Describe the morphology of the red blood cells.
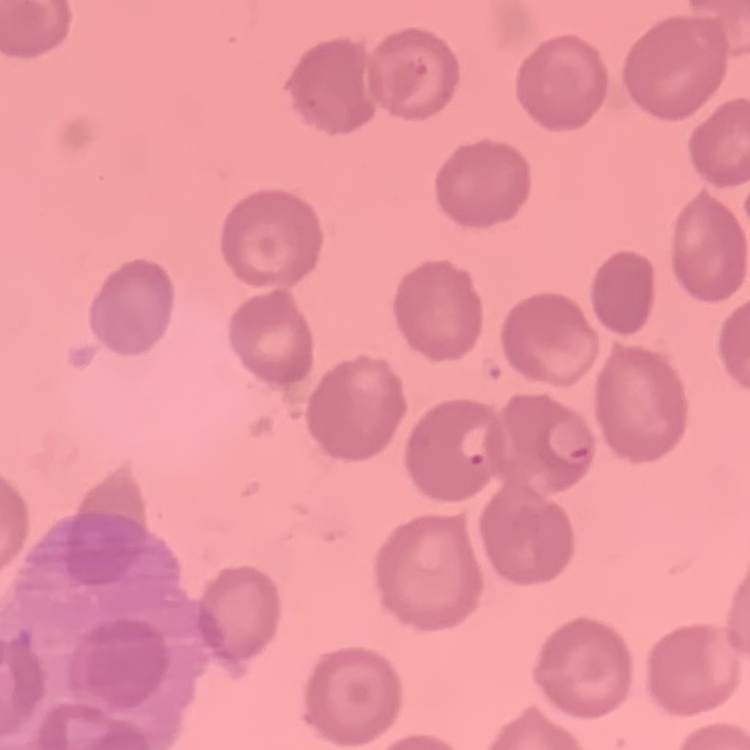
They show no rouleaux formation.

Field's or Giemsa stain. Square crop of a larger photomicrograph. Thin blood smear.